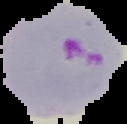

Summary:
  - Image size: 127×124 pixels
  - Malaria status: parasitized
  - Preparation: thin blood film
  - Image type: segmented cell region with the area outside set to black